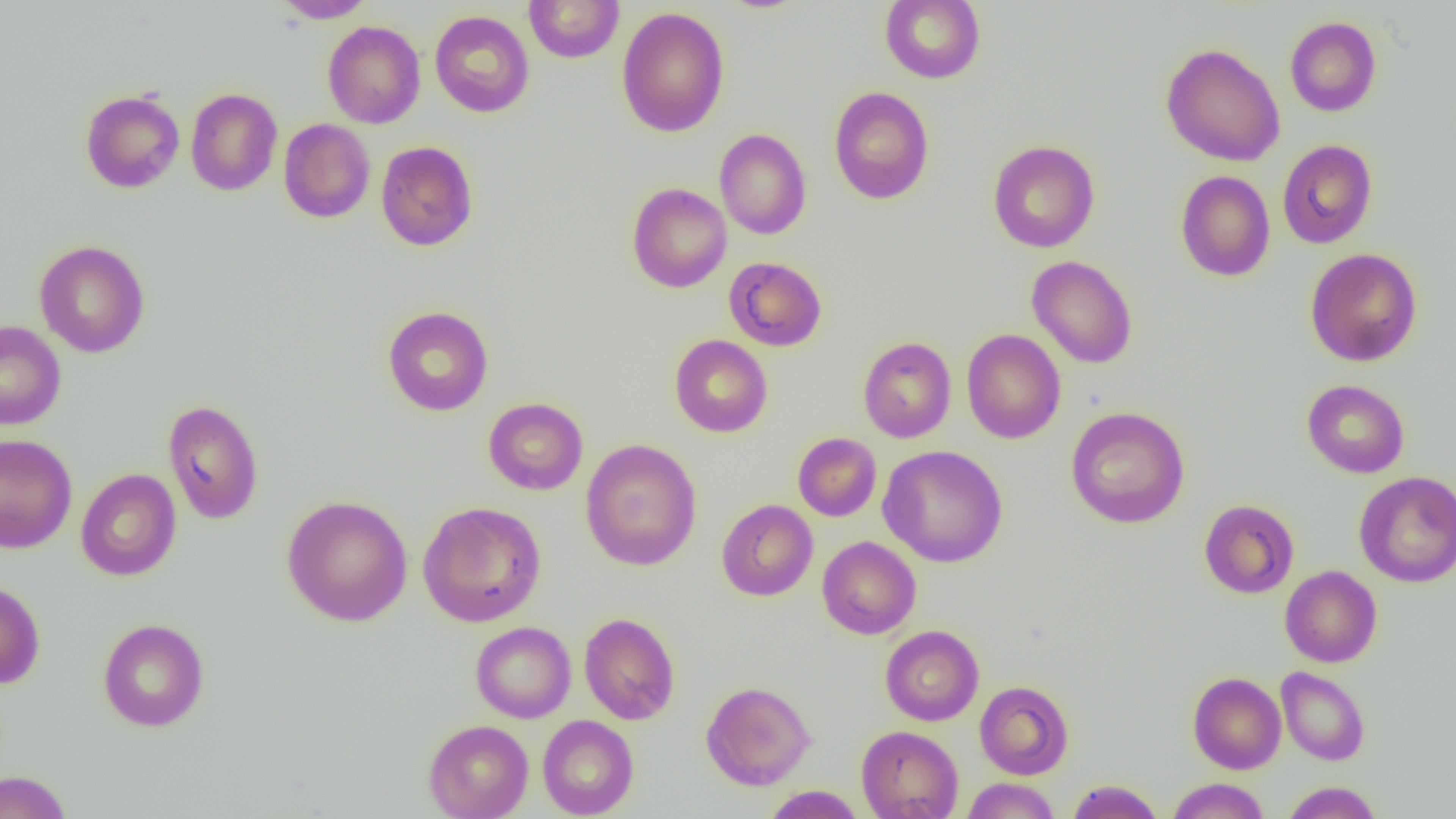
slide-level diagnosis = negative for blood parasites
modality = light microscopy
field of view = single
magnification = 1000x
image size = 1456×819 pixels
uninfected red blood cell locations = approximate bounding boxes as named x1/y1/x2/y2 corners in pixels: (x1=273, y1=0, x2=375, y2=22), (x1=880, y1=0, x2=985, y2=84), (x1=524, y1=1, x2=624, y2=63), (x1=616, y1=7, x2=730, y2=137), (x1=430, y1=10, x2=534, y2=117), (x1=1285, y1=16, x2=1381, y2=116), (x1=323, y1=21, x2=425, y2=128), (x1=1161, y1=43, x2=1285, y2=166), (x1=829, y1=87, x2=934, y2=205), (x1=185, y1=88, x2=282, y2=196), (x1=80, y1=89, x2=185, y2=193), (x1=279, y1=118, x2=375, y2=222), (x1=714, y1=129, x2=811, y2=239), (x1=987, y1=139, x2=1100, y2=252), (x1=376, y1=140, x2=478, y2=251), (x1=1277, y1=140, x2=1377, y2=248), (x1=1175, y1=170, x2=1275, y2=281), (x1=627, y1=183, x2=732, y2=293), (x1=35, y1=240, x2=150, y2=358), (x1=1304, y1=248, x2=1422, y2=366), (x1=1027, y1=255, x2=1138, y2=369), (x1=724, y1=257, x2=827, y2=351), (x1=382, y1=306, x2=494, y2=415), (x1=0, y1=321, x2=66, y2=430), (x1=962, y1=329, x2=1066, y2=444), (x1=670, y1=334, x2=773, y2=437), (x1=858, y1=337, x2=956, y2=442), (x1=1302, y1=380, x2=1409, y2=478), (x1=483, y1=397, x2=588, y2=495), (x1=163, y1=399, x2=264, y2=524), (x1=1066, y1=406, x2=1190, y2=528), (x1=793, y1=432, x2=881, y2=521), (x1=0, y1=434, x2=77, y2=553), (x1=580, y1=438, x2=702, y2=571), (x1=879, y1=444, x2=1008, y2=567), (x1=75, y1=468, x2=181, y2=581), (x1=1355, y1=471, x2=1456, y2=588), (x1=282, y1=495, x2=412, y2=626), (x1=716, y1=499, x2=818, y2=601), (x1=1199, y1=499, x2=1299, y2=598), (x1=418, y1=501, x2=546, y2=627), (x1=817, y1=536, x2=921, y2=639), (x1=1280, y1=565, x2=1382, y2=667), (x1=0, y1=580, x2=45, y2=689), (x1=579, y1=612, x2=680, y2=725), (x1=98, y1=618, x2=210, y2=732), (x1=470, y1=621, x2=576, y2=722), (x1=880, y1=625, x2=983, y2=725), (x1=1276, y1=666, x2=1369, y2=765), (x1=1188, y1=672, x2=1286, y2=774), (x1=701, y1=681, x2=815, y2=790), (x1=975, y1=681, x2=1073, y2=779), (x1=538, y1=715, x2=639, y2=818), (x1=423, y1=719, x2=533, y2=819), (x1=856, y1=725, x2=963, y2=819), (x1=0, y1=771, x2=72, y2=819), (x1=961, y1=777, x2=1060, y2=818), (x1=1167, y1=778, x2=1270, y2=819), (x1=1066, y1=780, x2=1164, y2=819), (x1=1283, y1=781, x2=1383, y2=819), (x1=763, y1=786, x2=865, y2=818)
preparation = thin blood smear